Locate every leukocyte (white blood cell).
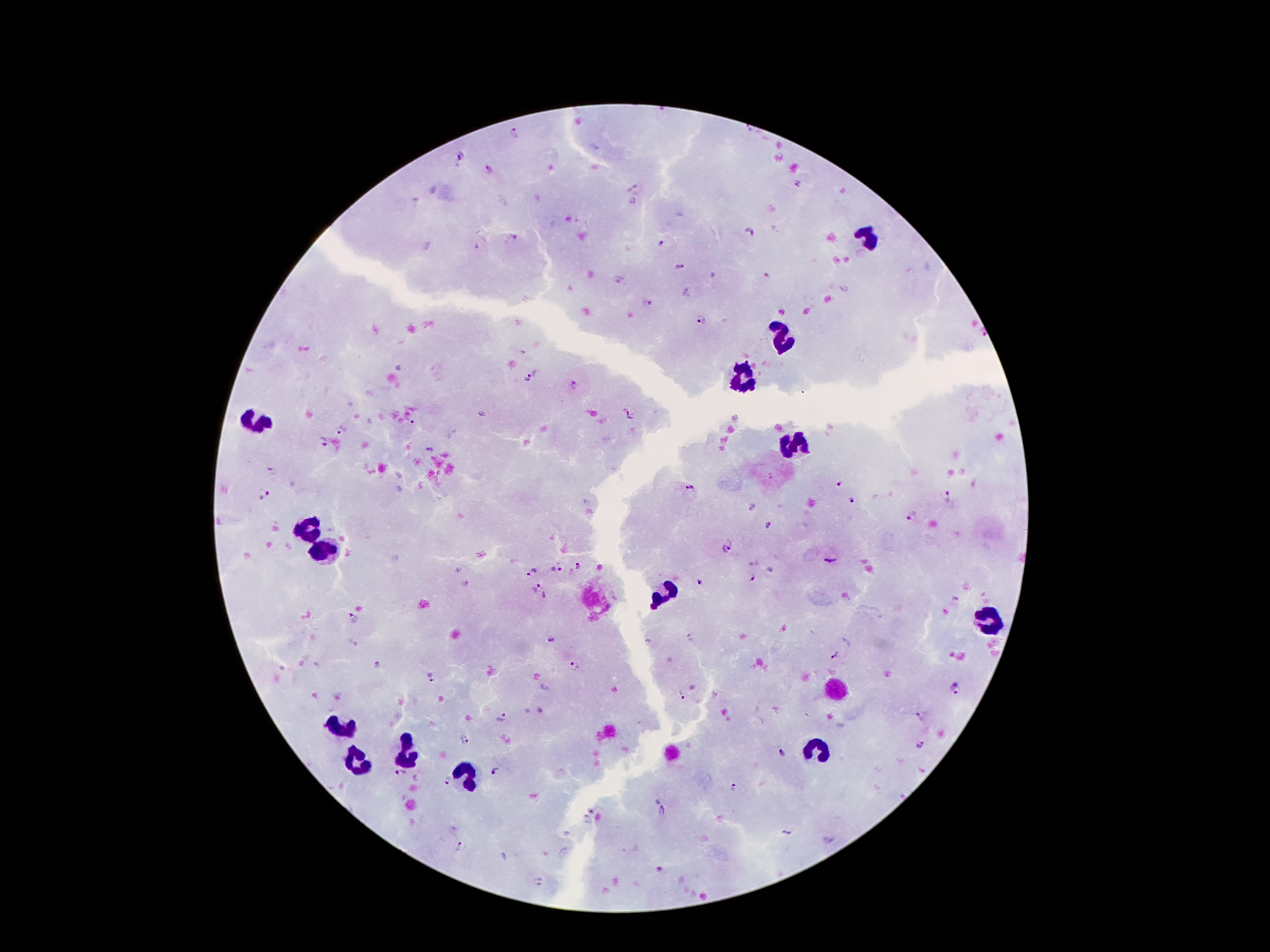
Approximate centers as (x, y) in pixels.
Leukocytes: (868, 237), (782, 338), (743, 379), (258, 422), (794, 444), (308, 532), (324, 553), (666, 594), (990, 621), (345, 725), (819, 752), (408, 754), (359, 762), (465, 774).

Summary:
  - Malaria parasite locations: (514, 132), (459, 154), (490, 169), (798, 183), (747, 232), (512, 238), (660, 243), (680, 268), (647, 303), (701, 321), (528, 378), (573, 385), (630, 416), (342, 429), (322, 442), (430, 450), (271, 470), (838, 486), (691, 487), (262, 494), (948, 495), (852, 500), (751, 505), (914, 514), (768, 525), (724, 548), (833, 561), (578, 567), (556, 569), (532, 573), (753, 578), (698, 580), (537, 587), (352, 620), (551, 638), (690, 639), (836, 659), (378, 664), (574, 666), (432, 677), (955, 689), (682, 696), (502, 717), (919, 718), (465, 739), (920, 745), (783, 752), (495, 770), (401, 774), (447, 780), (732, 788), (662, 811), (786, 832), (460, 848)
  - Capture: smartphone camera through the microscope eyepiece
  - Preparation: thick blood smear
  - Field of view: one from this slide
  - Patient malaria status: positive for Plasmodium falciparum
  - Magnification: 100x
  - Image size: 1270×952 pixels
  - Stain: Giemsa